Classify this cell by malaria status.
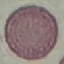

Uninfected.

capture = smartphone camera at the microscope eyepiece
stain = Giemsa
image type = automatically extracted cell patch, resized to 64 × 64 pixels
preparation = thin smear